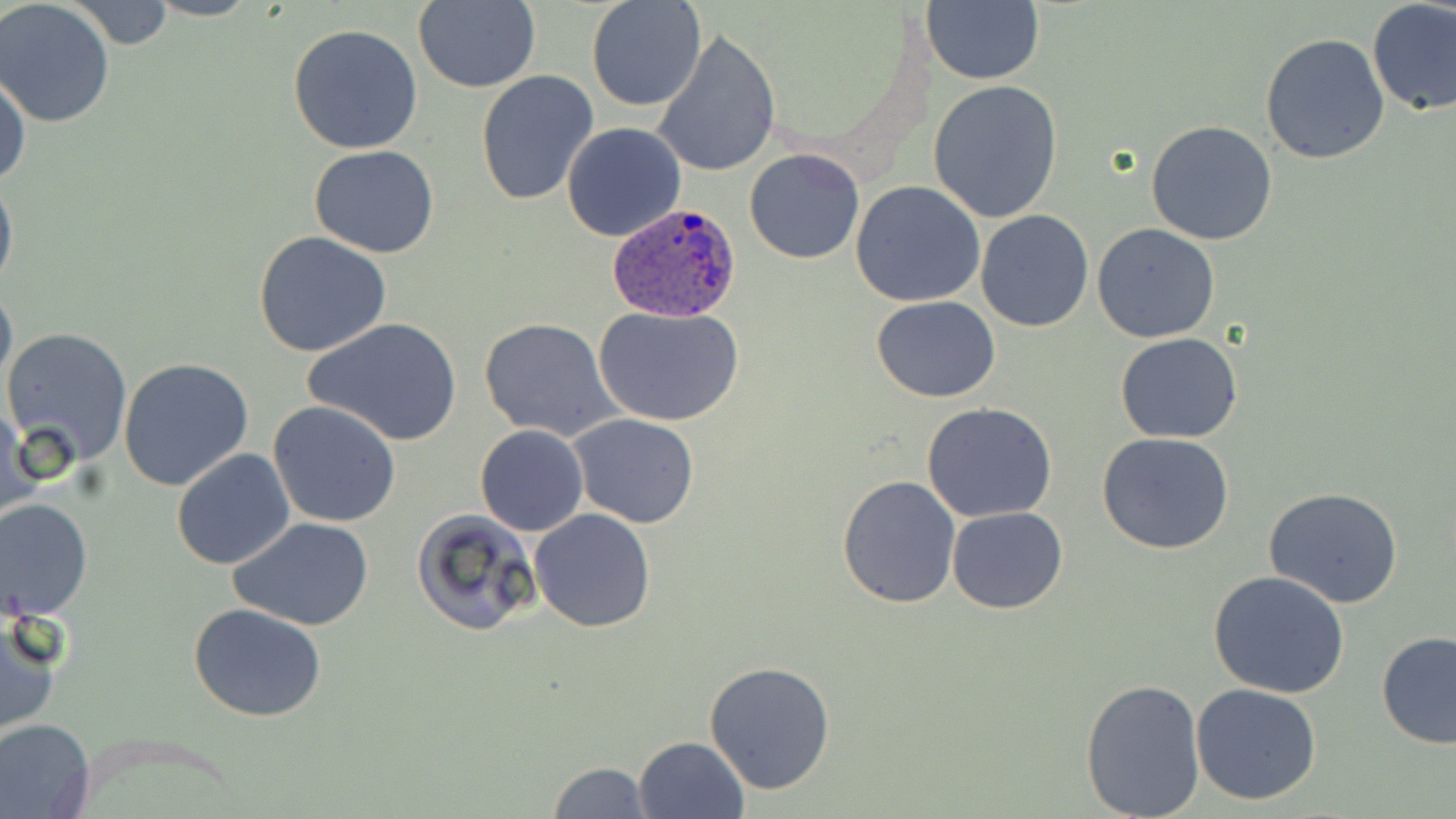
{
  "slide_level_diagnosis": "Plasmodium ovale",
  "magnification": "1000x",
  "uninfected_red_blood_cell_locations": "approximate bounding boxes as named x1/y1/x2/y2 corners in pixels: (x1=412, y1=0, x2=541, y2=92), (x1=922, y1=0, x2=1043, y2=86), (x1=68, y1=1, x2=179, y2=51), (x1=587, y1=1, x2=706, y2=112), (x1=1365, y1=1, x2=1455, y2=115), (x1=0, y1=2, x2=117, y2=126), (x1=287, y1=23, x2=423, y2=154), (x1=652, y1=28, x2=781, y2=179), (x1=1261, y1=32, x2=1390, y2=165), (x1=0, y1=69, x2=30, y2=190), (x1=475, y1=72, x2=601, y2=209), (x1=927, y1=79, x2=1065, y2=223), (x1=1146, y1=119, x2=1279, y2=245), (x1=562, y1=121, x2=687, y2=243), (x1=308, y1=146, x2=440, y2=258), (x1=743, y1=147, x2=865, y2=265), (x1=0, y1=166, x2=18, y2=299), (x1=851, y1=181, x2=986, y2=306), (x1=974, y1=209, x2=1093, y2=332), (x1=1092, y1=224, x2=1220, y2=344), (x1=253, y1=231, x2=393, y2=358), (x1=0, y1=276, x2=16, y2=401), (x1=871, y1=296, x2=1001, y2=402), (x1=592, y1=305, x2=746, y2=426), (x1=303, y1=316, x2=461, y2=448), (x1=477, y1=316, x2=625, y2=444), (x1=1, y1=326, x2=134, y2=468), (x1=1116, y1=333, x2=1243, y2=443), (x1=118, y1=357, x2=255, y2=492), (x1=268, y1=401, x2=402, y2=530), (x1=922, y1=402, x2=1058, y2=521), (x1=1, y1=404, x2=38, y2=529), (x1=569, y1=414, x2=700, y2=529), (x1=475, y1=424, x2=589, y2=537), (x1=1096, y1=433, x2=1237, y2=555), (x1=172, y1=448, x2=294, y2=569), (x1=836, y1=476, x2=963, y2=609), (x1=1263, y1=489, x2=1406, y2=609), (x1=0, y1=497, x2=94, y2=621), (x1=948, y1=507, x2=1068, y2=614), (x1=529, y1=508, x2=656, y2=632), (x1=411, y1=509, x2=542, y2=638), (x1=230, y1=518, x2=376, y2=632), (x1=200, y1=528, x2=359, y2=713), (x1=1207, y1=570, x2=1353, y2=699), (x1=187, y1=603, x2=329, y2=722), (x1=0, y1=610, x2=63, y2=739), (x1=1374, y1=631, x2=1456, y2=750), (x1=703, y1=662, x2=837, y2=796), (x1=1080, y1=676, x2=1206, y2=817), (x1=1191, y1=682, x2=1323, y2=805), (x1=0, y1=717, x2=96, y2=818), (x1=634, y1=736, x2=750, y2=819), (x1=544, y1=760, x2=653, y2=818)",
  "plasmodium_ovale_infected_red_blood_cell_locations": "approximate bounding boxes as named x1/y1/x2/y2 corners in pixels: (x1=608, y1=200, x2=742, y2=322)",
  "image_size": "1456×819 pixels",
  "field_of_view": "single",
  "stain": "May-Grünwald-Giemsa",
  "preparation": "thin blood film",
  "modality": "light microscopy"
}